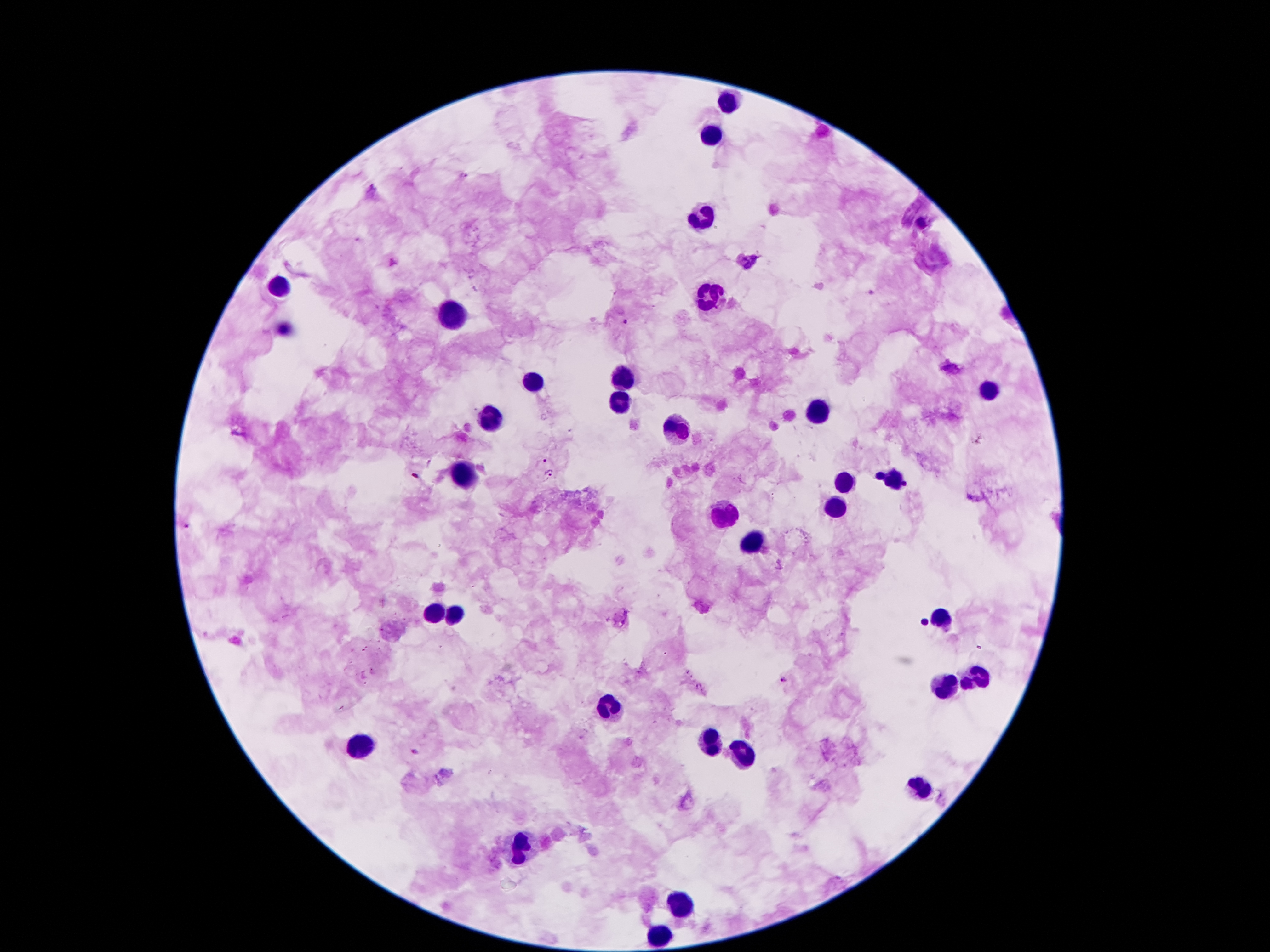
coordinate format = approximate object centers, in pixels from the top-left corner
Plasmodium parasite locations = (x=464, y=174), (x=371, y=188), (x=624, y=321), (x=546, y=460), (x=549, y=476), (x=186, y=524), (x=786, y=680), (x=416, y=752)
leukocyte locations = (x=730, y=101), (x=710, y=135), (x=702, y=213), (x=278, y=290), (x=709, y=299), (x=453, y=317), (x=623, y=380), (x=534, y=383), (x=990, y=390), (x=621, y=404), (x=821, y=413), (x=492, y=423), (x=672, y=430), (x=464, y=477), (x=894, y=477), (x=847, y=481), (x=836, y=507), (x=723, y=514), (x=752, y=542), (x=430, y=612), (x=457, y=614), (x=940, y=619), (x=975, y=677), (x=947, y=687), (x=609, y=707), (x=710, y=743), (x=360, y=750), (x=744, y=756), (x=917, y=787), (x=520, y=850), (x=682, y=901), (x=661, y=936)
preparation = thick blood film
image size = 1270×952 pixels
patient malaria status = positive for Plasmodium falciparum
magnification = 100x
capture = smartphone camera through the microscope eyepiece
stain = Giemsa
field of view = one from this slide